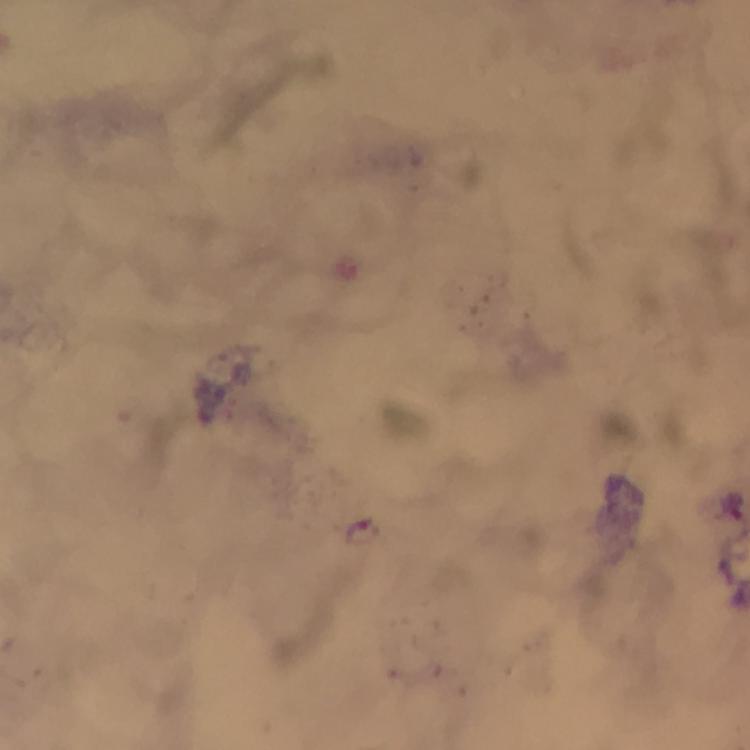

Approximate centers as (x, y) in pixels.
Summary:
  - Plasmodium parasite locations: (734, 506), (363, 533)
  - Capture: smartphone mounted on the microscope
  - Cropped from: one field of view
  - Context: from a diagnostic examination for malaria
  - Preparation: thick blood smear
  - Magnification: 100x
  - Image size: 750×750 pixels
  - Immersion oil: used
  - Stain: Giemsa